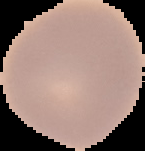

Result: no Plasmodium parasites seen. Image is 145×151 pixels. Segmented cell region on a black background. From a thin blood film.